Name the parasite shown.
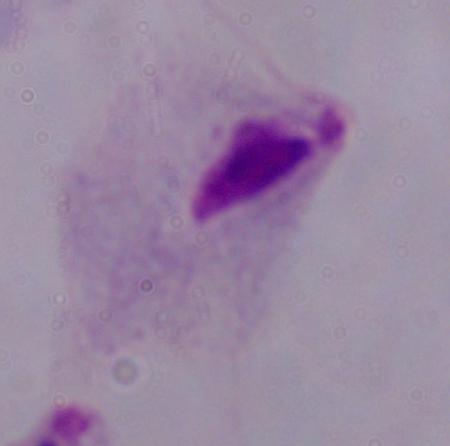
A trichomonad.

Summary:
  - Modality: photomicrograph
  - Magnification: 1000x